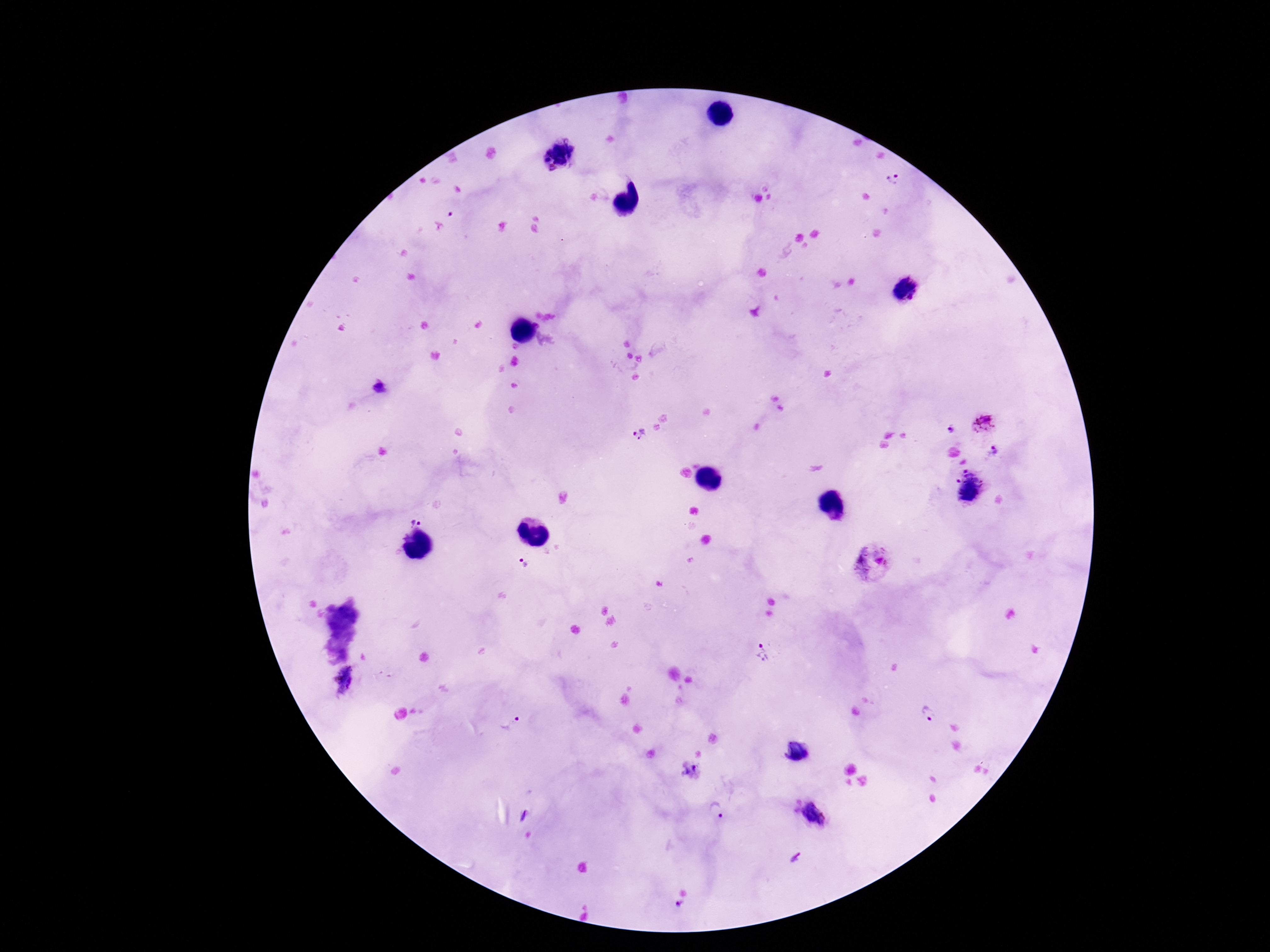
Approximate centers as (x, y) in pixels. Plasmodium parasite locations: (558, 154), (892, 179), (904, 290), (380, 388), (984, 422), (950, 430), (640, 435), (994, 451), (969, 486), (417, 518), (872, 563), (523, 567), (763, 656), (346, 681), (929, 714), (510, 723), (796, 751), (690, 770), (717, 810), (813, 816), (797, 857), (680, 903). Image is 1270×952 pixels. 100x magnification. Giemsa stain. Thick blood smear. Smartphone photograph taken through the microscope eyepiece. Patient malaria status: positive. Single field of view.